Name the parasite shown.
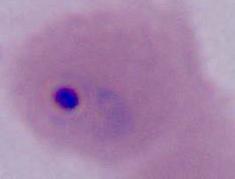
Plasmodium.

modality = micrograph
magnification = 400x or 1000x